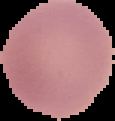
Summary:
  - Image size: 115×121 pixels
  - Malaria status: uninfected
  - Image type: cell region segmented out of the field of view; surrounding area masked to black
  - Preparation: thin blood film